Identify the parasite.
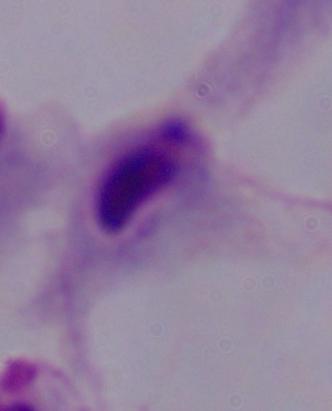
This is a trichomonad.

Captured at 1000x magnification. Micrograph.